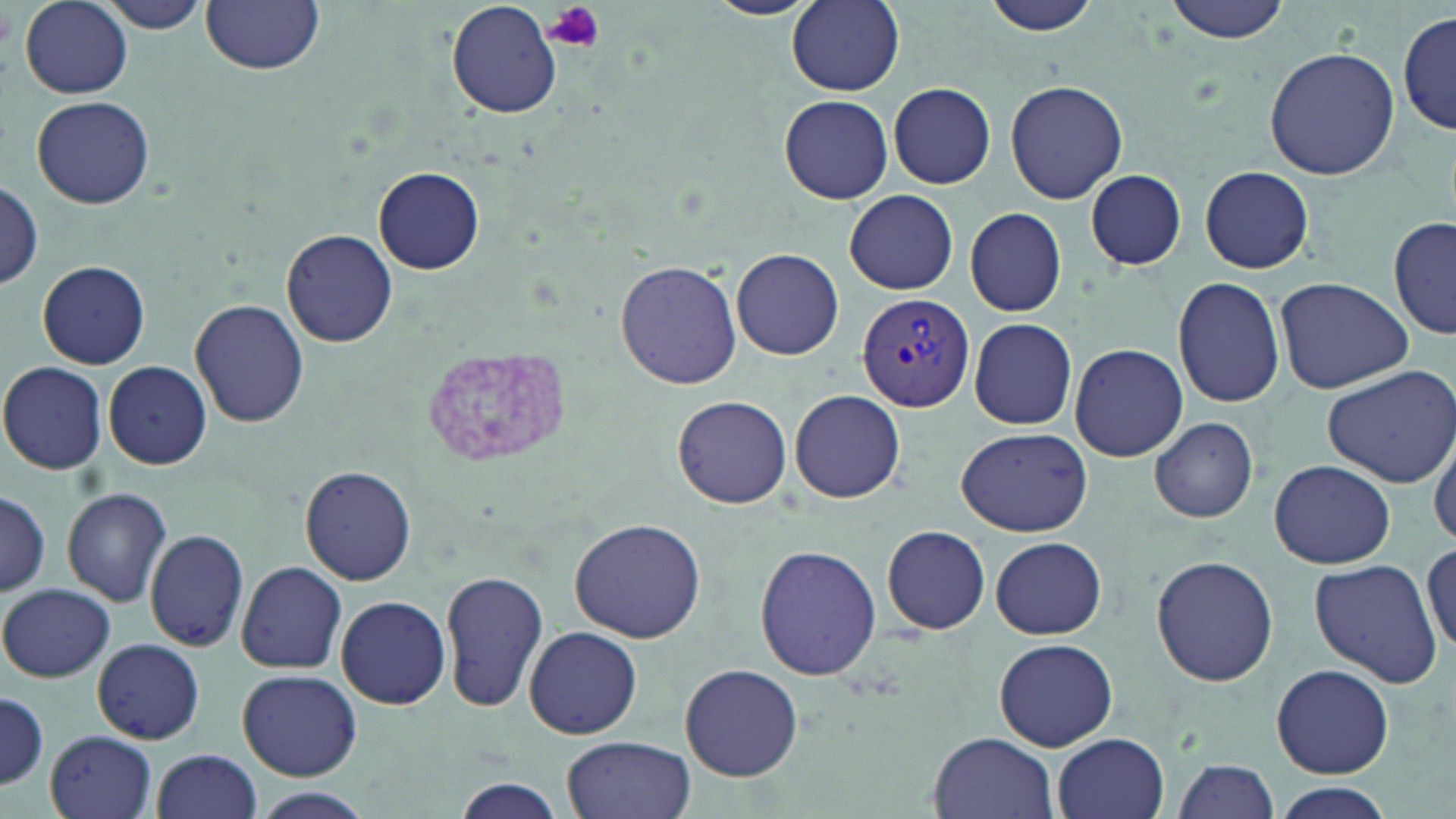

Approximate bounding boxes as [x1, y1, x2, y2] in pixels. Plasmodium vivax-infected red blood cell locations: [856, 294, 975, 410]. Platelet locations: [541, 0, 607, 54]. Uninfected red blood cell locations: [98, 0, 216, 34], [201, 0, 325, 75], [703, 0, 816, 20], [787, 0, 904, 95], [980, 0, 1101, 37], [1162, 0, 1290, 43], [19, 1, 133, 98], [447, 1, 563, 118], [1398, 12, 1454, 136], [1264, 47, 1400, 180], [1005, 79, 1128, 205], [889, 82, 995, 189], [779, 94, 892, 203], [32, 96, 155, 209], [1199, 166, 1315, 273], [374, 168, 484, 273], [1083, 168, 1187, 271], [0, 181, 44, 290], [844, 189, 958, 294], [964, 207, 1066, 316], [1389, 212, 1456, 342], [283, 229, 398, 346], [732, 248, 844, 360], [615, 258, 743, 391], [39, 259, 150, 369], [1173, 277, 1285, 408], [1272, 277, 1413, 394], [190, 299, 309, 428], [969, 318, 1078, 430], [1069, 344, 1187, 462], [0, 361, 110, 474], [103, 361, 213, 470], [1322, 363, 1456, 491], [789, 390, 906, 503], [671, 394, 793, 509], [1150, 417, 1259, 524], [955, 427, 1093, 538], [1430, 434, 1456, 548], [1268, 460, 1396, 569], [300, 465, 416, 584], [62, 487, 173, 607], [0, 491, 50, 596], [568, 517, 706, 645], [880, 525, 992, 636], [145, 530, 249, 651], [990, 536, 1107, 639], [1425, 541, 1456, 658], [754, 544, 881, 682], [1150, 555, 1277, 688], [1308, 559, 1441, 687], [235, 562, 349, 674], [440, 569, 549, 713], [1, 583, 113, 683], [335, 595, 451, 710], [522, 625, 645, 740], [93, 638, 205, 744], [993, 638, 1117, 751], [679, 663, 803, 781], [1271, 663, 1394, 778], [237, 669, 362, 781], [0, 692, 48, 790], [46, 731, 157, 819], [929, 732, 1059, 819], [1053, 733, 1169, 819], [560, 735, 694, 819], [151, 750, 262, 819], [1170, 758, 1281, 818], [450, 778, 569, 819], [1271, 784, 1396, 817], [246, 787, 375, 819]. Slide-level diagnosis: Plasmodium vivax. May-Grünwald-Giemsa-stained preparation. Captured at 1000x magnification. Image is 1456×819 pixels. Thin blood film. Light microscopy. One field of a larger specimen.